State which parasite is depicted.
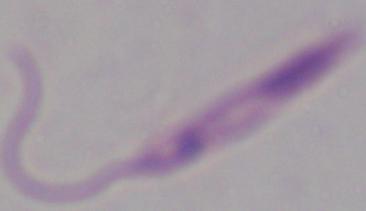

Leishmania.

Captured at 1000x magnification. Photomicrograph.